State the preparation type.
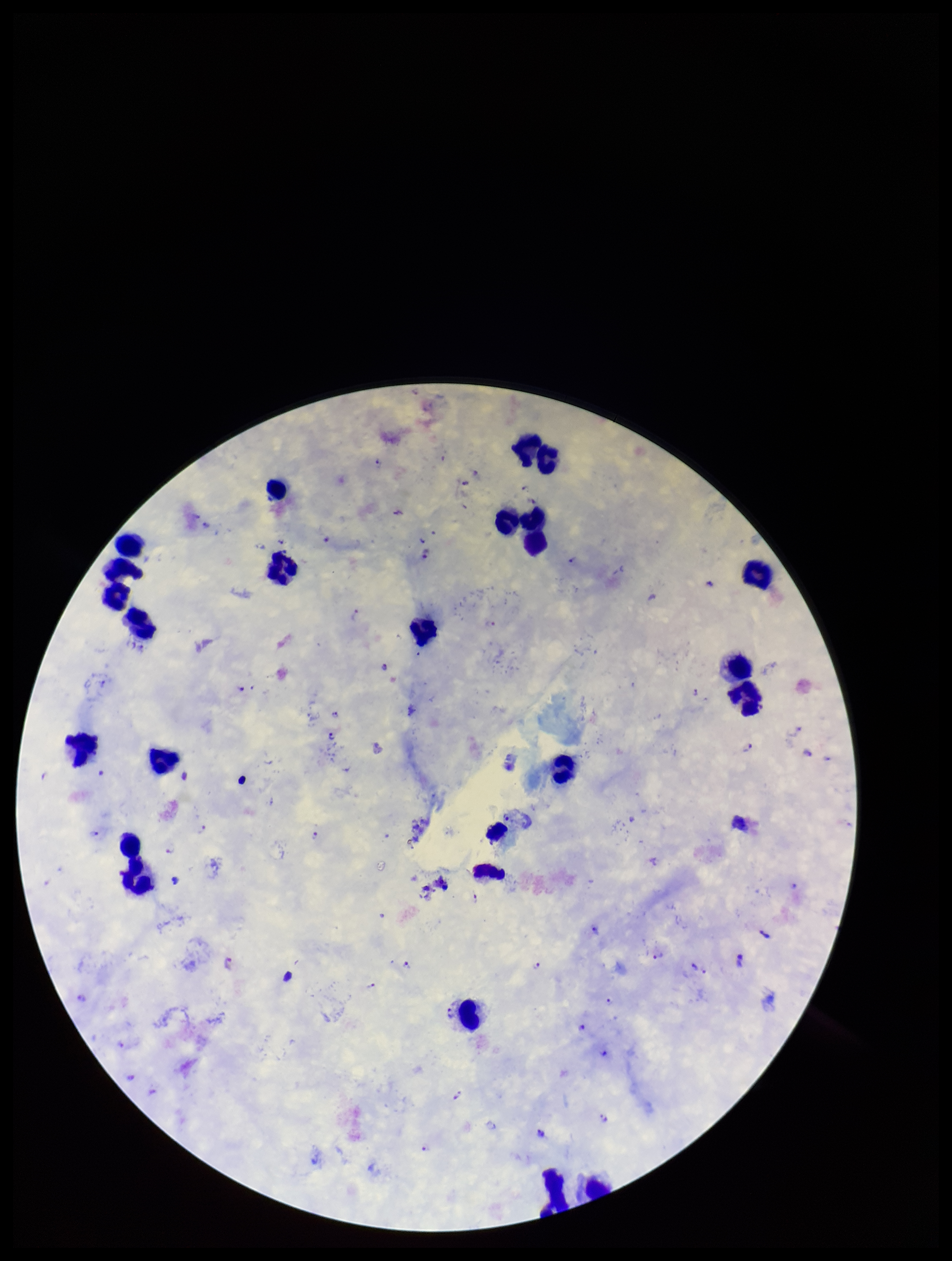

Thick.

plasmodium_parasites: detected
stain: Giemsa
capture: smartphone photograph through the microscope eyepiece
leukocyte_count: 17
field_of_view: one from this slide
image_size: 952×1261 pixels
patient_malaria_status: infected
parasite_count: 29
species_reported_for_this_patient: Plasmodium falciparum